Outline each blood parasite and name the species.
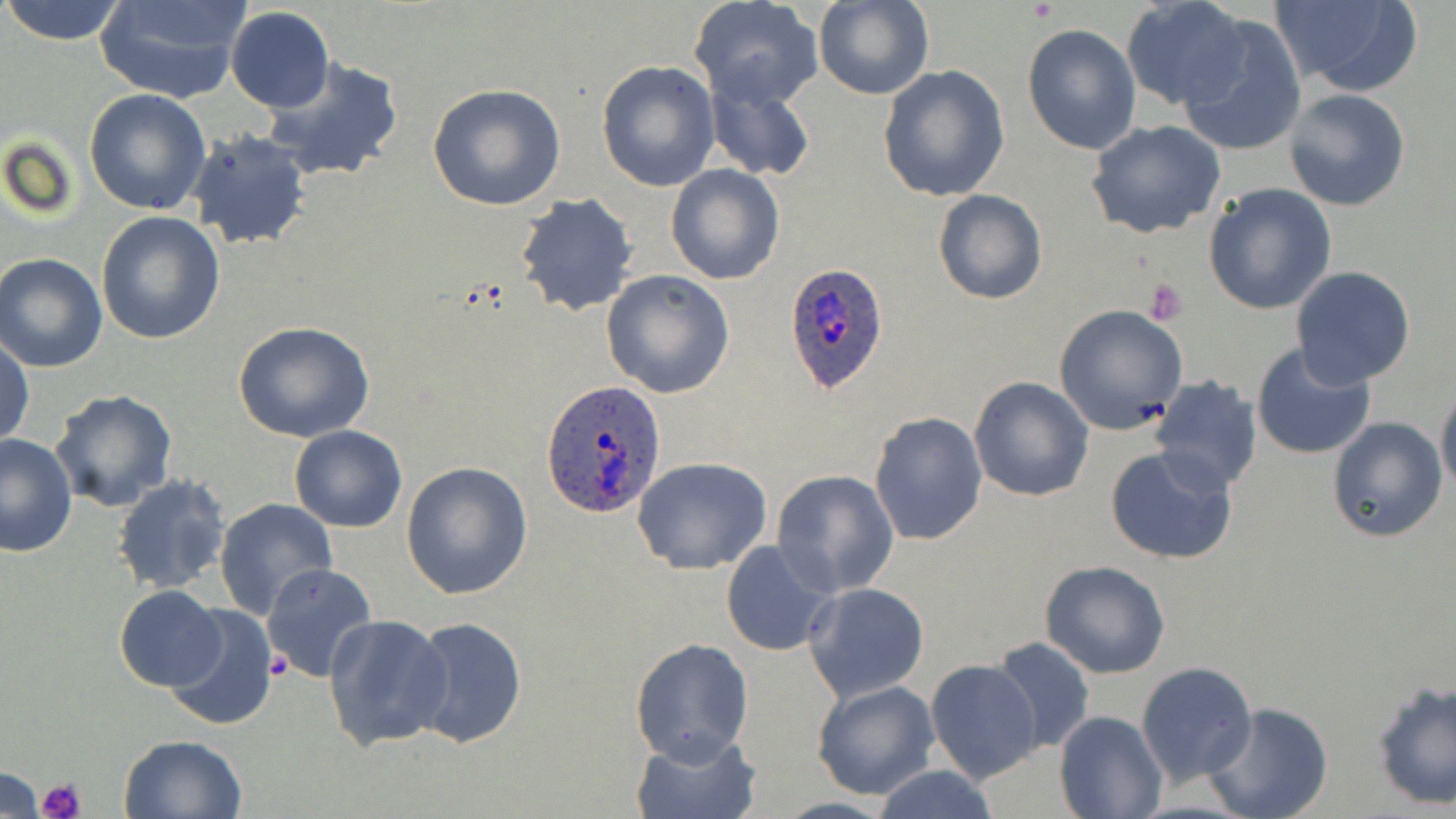

Approximate bounding boxes as (x1, y1, x2, y2) in pixels.
Plasmodium ovale-infected red blood cells: (783, 263, 894, 397), (541, 382, 668, 517).
No Plasmodium falciparum, Plasmodium malariae, Plasmodium vivax, Babesia divergens, or Trypanosoma brucei observed.

slide-level diagnosis = Plasmodium ovale
magnification = 1000x
preparation = thin blood film
image size = 1456×819 pixels
platelet locations = approximate bounding boxes as (x1, y1, x2, y2) in pixels: (1144, 277, 1189, 324), (36, 777, 86, 819)
uninfected red blood cell locations = approximate bounding boxes as (x1, y1, x2, y2) in pixels: (0, 0, 129, 46), (93, 0, 246, 103), (813, 0, 933, 100), (689, 1, 823, 108), (1120, 1, 1250, 111), (1268, 1, 1422, 95), (226, 6, 334, 114), (1176, 15, 1308, 158), (1021, 24, 1141, 155), (260, 57, 405, 182), (596, 60, 720, 191), (877, 63, 1009, 202), (704, 75, 817, 184), (427, 84, 568, 211), (83, 88, 211, 216), (1282, 88, 1411, 212), (1085, 121, 1228, 240), (183, 126, 313, 252), (665, 163, 785, 285), (1204, 184, 1337, 316), (932, 190, 1048, 306), (514, 193, 639, 317), (95, 211, 224, 344), (0, 253, 108, 372), (1292, 267, 1416, 387), (601, 269, 734, 398), (1052, 304, 1189, 435), (233, 320, 375, 443), (0, 337, 34, 449), (1251, 341, 1378, 461), (968, 376, 1093, 501), (1149, 376, 1263, 492), (1436, 384, 1456, 497), (48, 388, 180, 513), (873, 395, 1089, 523), (869, 412, 988, 546), (1326, 416, 1447, 542), (289, 425, 407, 532), (0, 433, 77, 558), (1106, 445, 1239, 567), (632, 457, 772, 575), (400, 460, 532, 600), (772, 470, 900, 596), (111, 474, 233, 593), (214, 497, 339, 618), (721, 539, 838, 657), (1041, 561, 1169, 678), (262, 562, 378, 685), (802, 582, 929, 701), (114, 586, 225, 692), (163, 604, 278, 732), (323, 614, 452, 750), (403, 614, 529, 749), (630, 635, 753, 765), (990, 637, 1095, 754), (925, 658, 1043, 783), (1136, 661, 1257, 787), (811, 679, 940, 800), (1370, 679, 1456, 810), (1201, 701, 1335, 819), (1055, 711, 1167, 819), (633, 730, 759, 819), (117, 733, 249, 819), (868, 766, 999, 819), (0, 767, 46, 816)
modality = light microscopy
field of view = one of a larger specimen
stain = May-Grünwald-Giemsa